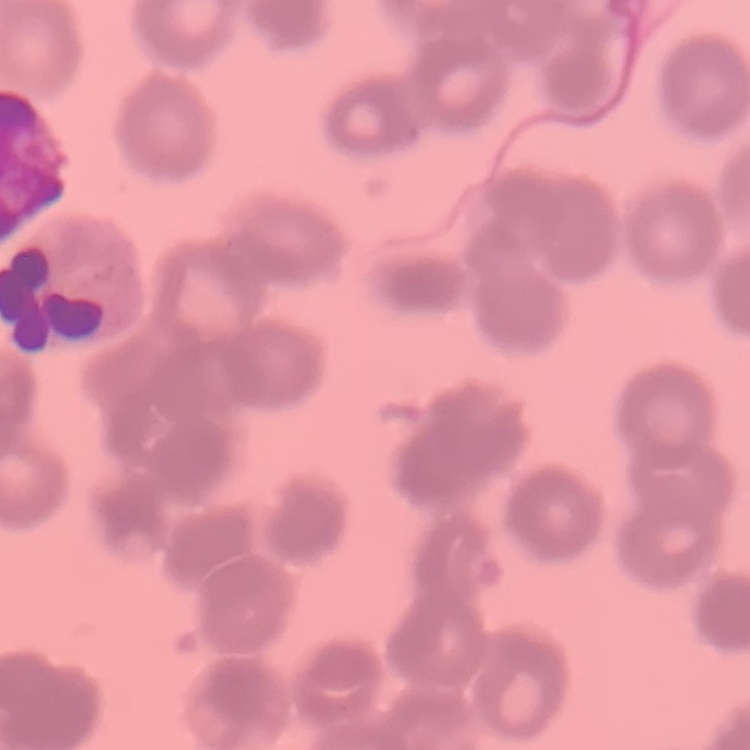

{
  "erythrocyte_morphology": "rouleaux formation",
  "preparation": "thin blood film",
  "stain": "Field's or Giemsa",
  "image_type": "one tile cut from a larger photomicrograph"
}